State which parasite is depicted.
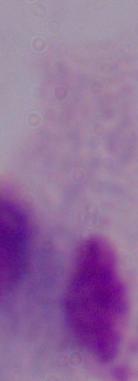
This is a trichomonad.

magnification = 1000x
modality = photomicrograph